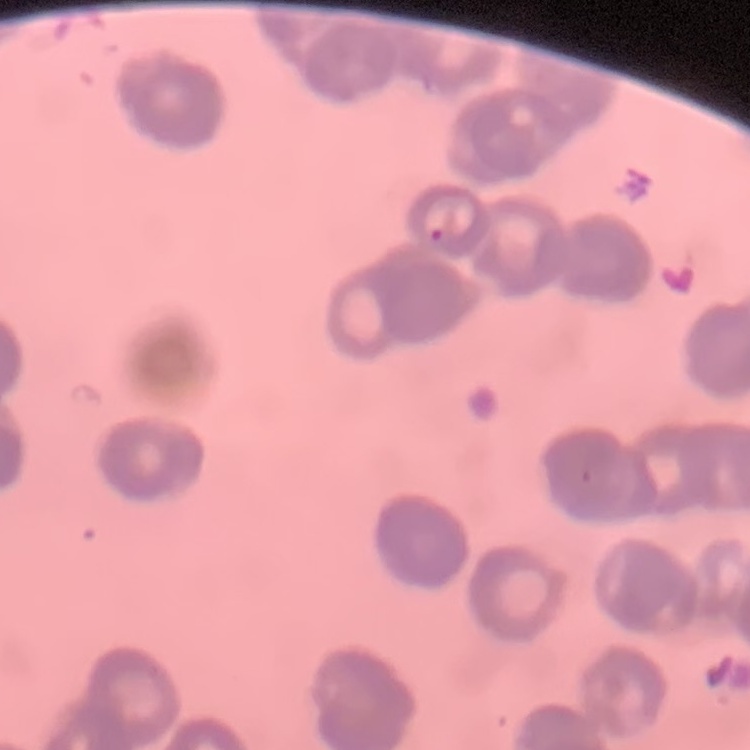

The erythrocytes exhibit rouleaux formation. One tile cut from a larger photomicrograph. Field's or Giemsa stain. Thin blood film.